Name the parasite shown.
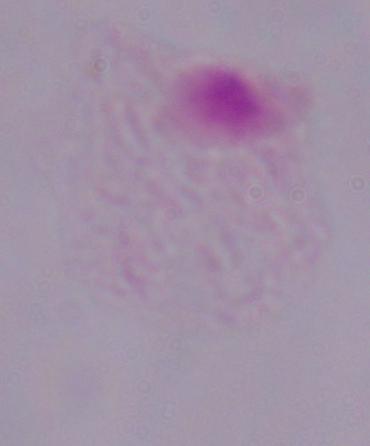
A trichomonad.

1000x magnification. Photomicrograph.